Locate every leukocyte (white blood cell).
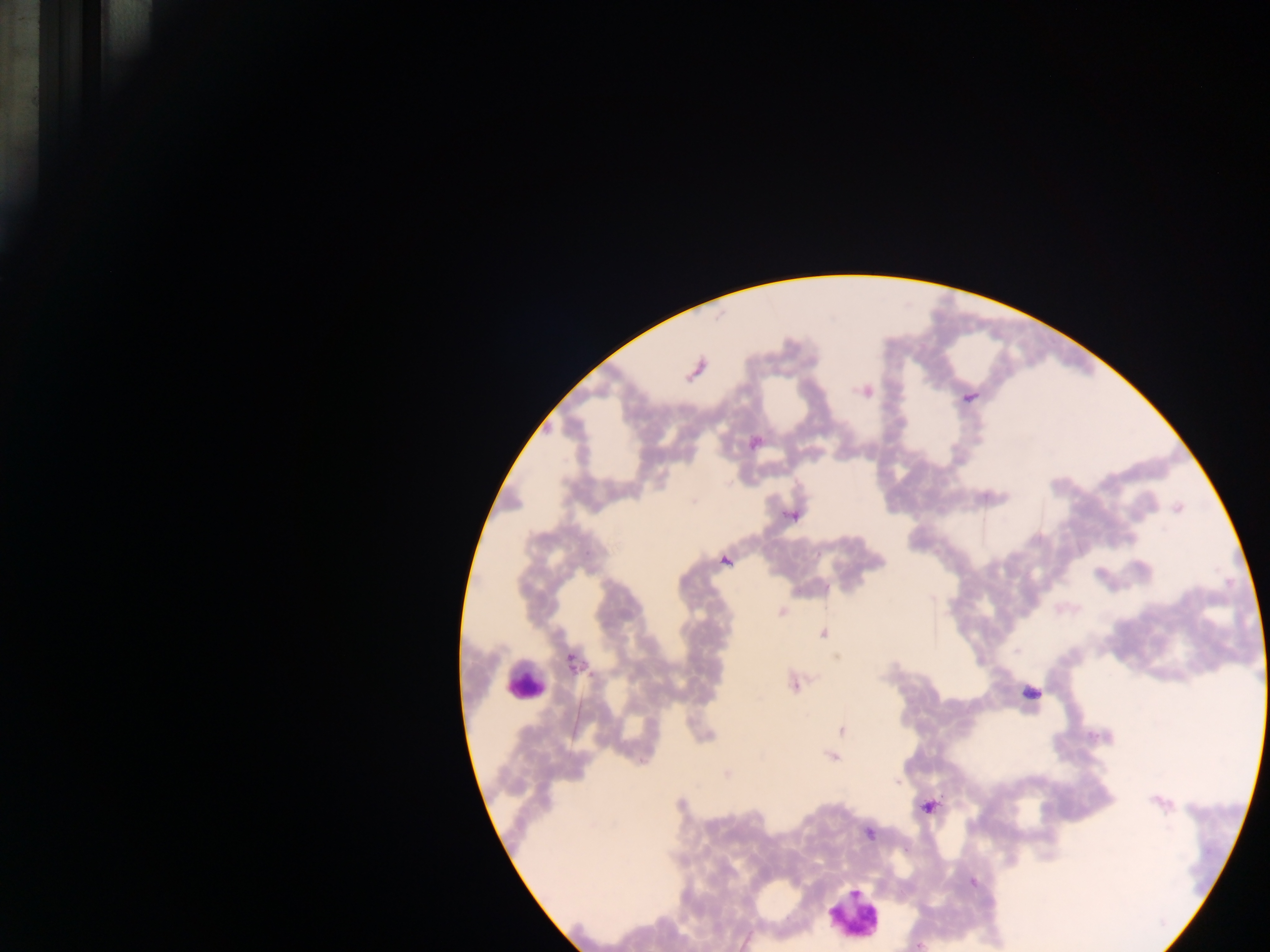

Approximate centers as [x, y] in pixels.
Leukocytes: [523, 682], [851, 912].

Summary:
  - Malaria parasite locations: [794, 685], [898, 781], [917, 946]
  - Field of view: single
  - Image size: 1270×952 pixels
  - Country: Ghana
  - Preparation: thick blood film
  - Capture: mobile-phone photograph through a microscope